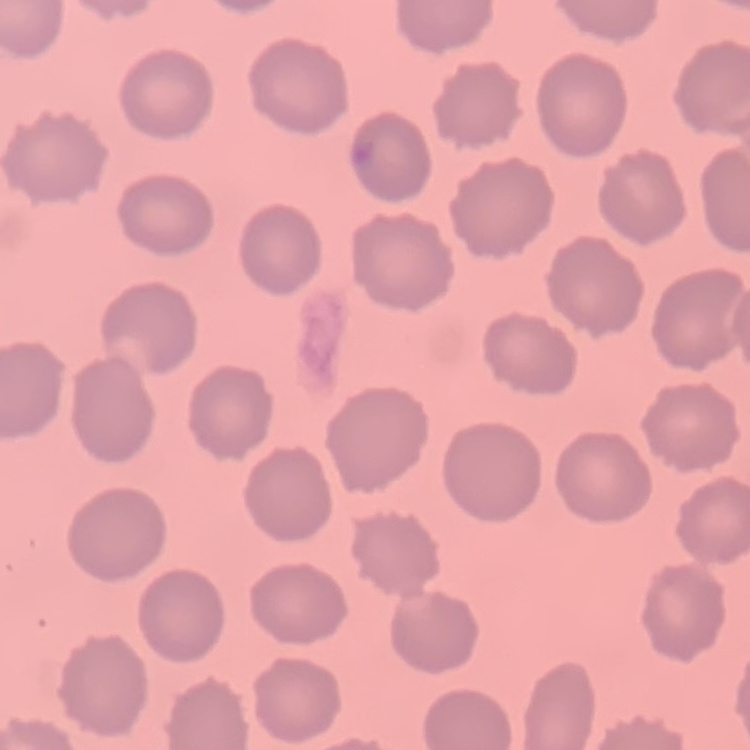

The erythrocytes exhibit no rouleaux formation. One tile cut from a larger photomicrograph. Thin blood smear. Stained with either Field's or Giemsa.